Give the position of every malaria parasite, noting whether each is a trophozoite, schizont, or gametocyte.
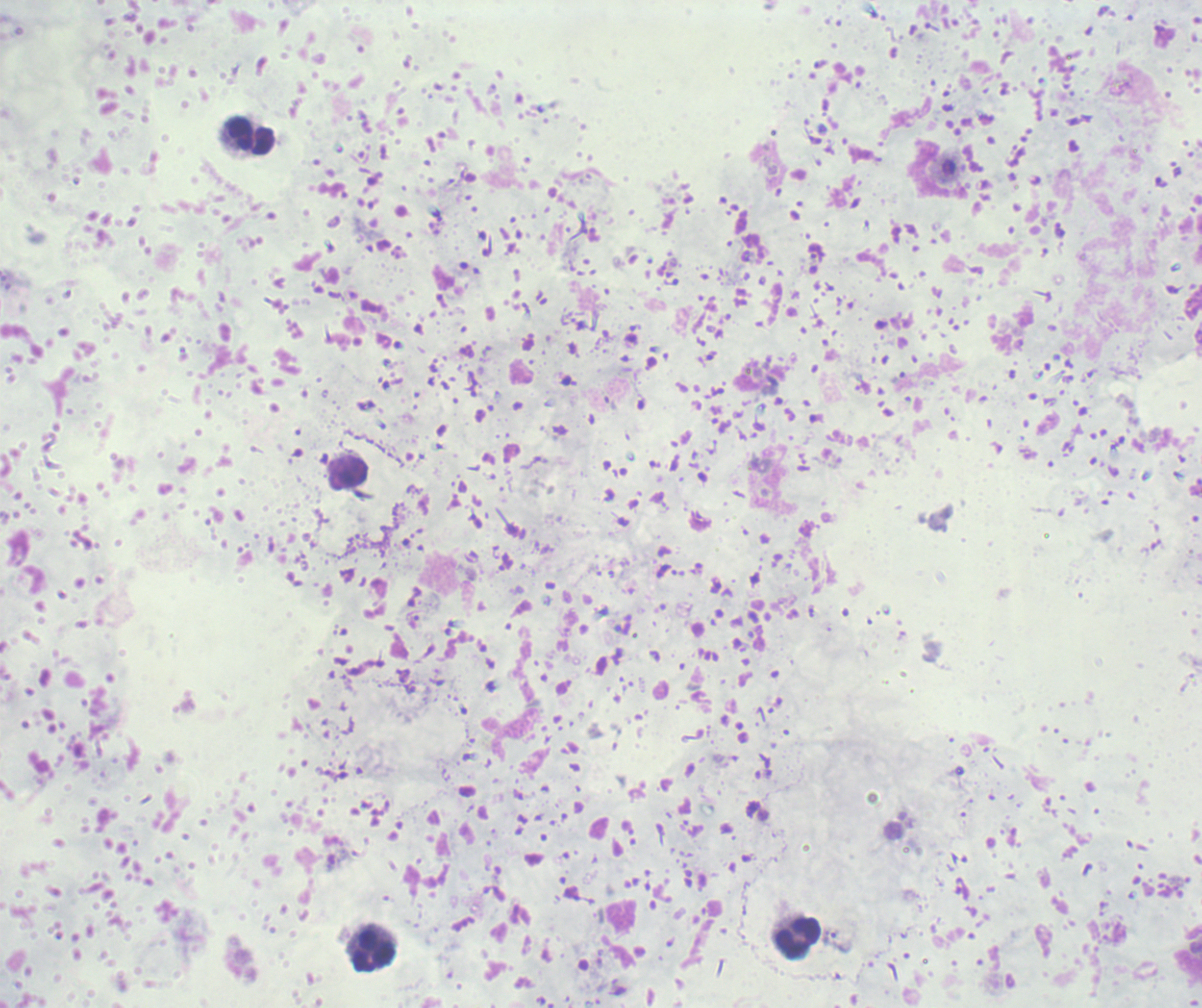
Negative for malaria parasites.

{
  "stain": "Romanowsky",
  "context": "previously used in a real diagnosis",
  "preparation": "thick blood smear",
  "leukocyte_locations": "approximate object centers, in pixels from the top-left corner: (x=251, y=136), (x=348, y=473), (x=798, y=939), (x=374, y=952)",
  "image_size": "1202×1008 pixels",
  "field_of_view": "single",
  "background_quality": "unsatisfactory",
  "magnification": "100x"
}